Outline each uninfected red blood cell.
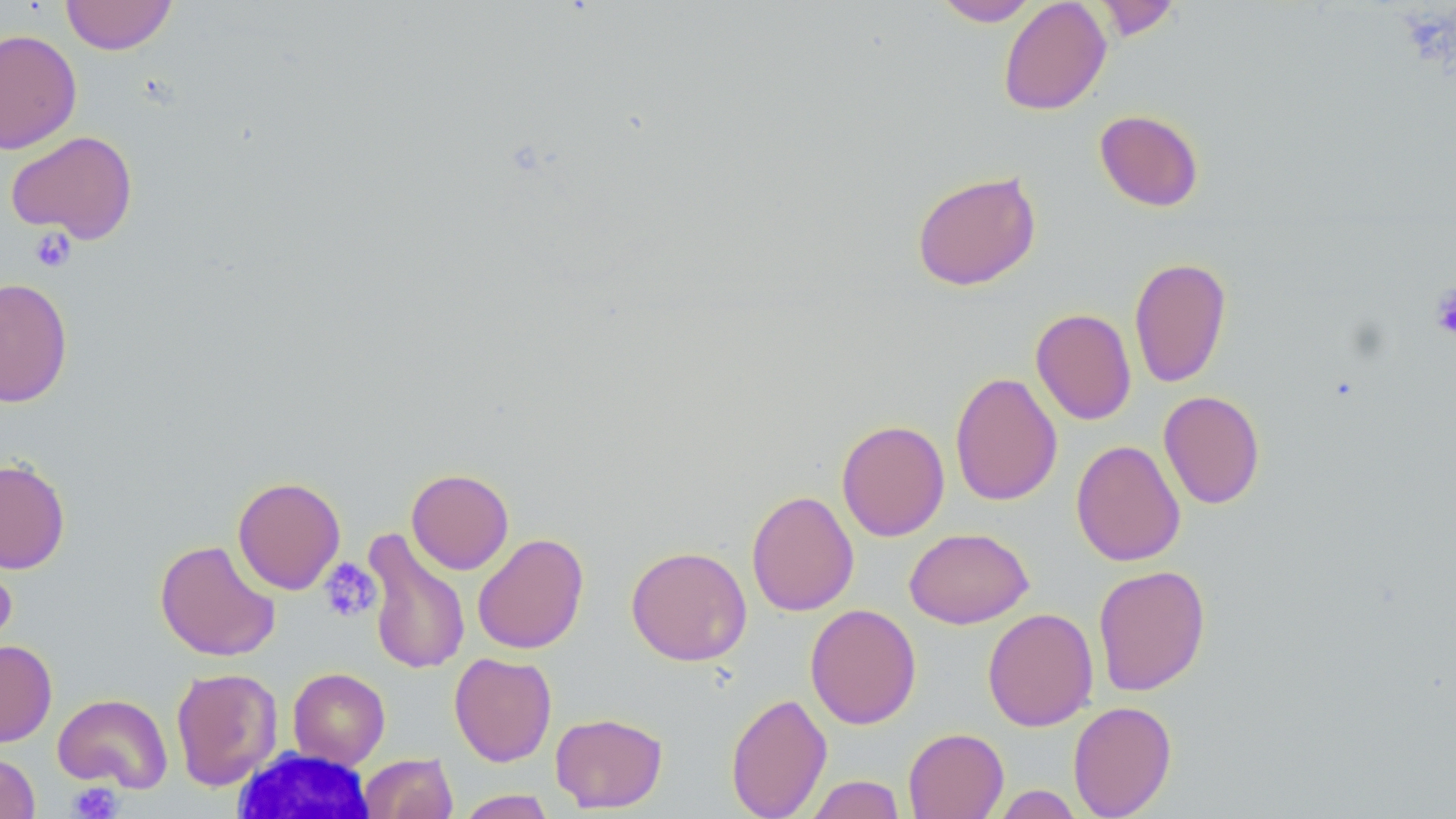
Approximate bounding boxes as (x1, y1, x2, y2) in pixels.
Uninfected red blood cells: (61, 0, 177, 55), (932, 0, 1040, 26), (998, 0, 1111, 116), (1093, 0, 1182, 41), (0, 28, 82, 154), (1094, 109, 1204, 211), (5, 130, 138, 244), (911, 170, 1042, 291), (1129, 256, 1231, 388), (0, 277, 73, 407), (1030, 308, 1137, 425), (949, 372, 1063, 507), (1158, 390, 1265, 509), (836, 419, 949, 541), (1070, 439, 1186, 566), (0, 457, 70, 574), (406, 468, 514, 575), (233, 476, 346, 595), (746, 490, 860, 616), (904, 527, 1034, 629), (362, 529, 471, 676), (473, 533, 589, 654), (154, 539, 281, 661), (625, 545, 752, 666), (0, 548, 17, 660), (1093, 564, 1211, 696), (805, 603, 922, 730), (982, 607, 1098, 731), (0, 639, 57, 747), (449, 652, 557, 767), (171, 667, 283, 791), (288, 667, 390, 769), (725, 692, 832, 819), (52, 693, 173, 792), (1068, 701, 1177, 818), (550, 712, 667, 813), (903, 727, 1009, 819), (0, 752, 40, 818), (359, 753, 457, 818), (804, 774, 907, 818), (990, 785, 1085, 818), (455, 790, 558, 818).

Summary:
  - Platelet locations: (28, 228, 76, 273), (1431, 283, 1456, 342), (318, 557, 382, 623), (67, 782, 123, 819)
  - White blood cell locations: (232, 747, 378, 818)
  - Slide-level diagnosis: no evidence of blood parasites
  - Image size: 1456×819 pixels
  - Field of view: one of a larger specimen
  - Magnification: 1000x
  - Preparation: thin blood smear
  - Stain: May-Grünwald-Giemsa
  - Modality: light microscopy